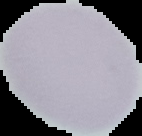

Summary:
  - Image size: 142×136 pixels
  - Image type: segmented cell region on a black background
  - Preparation: thin blood smear
  - Malaria status: uninfected